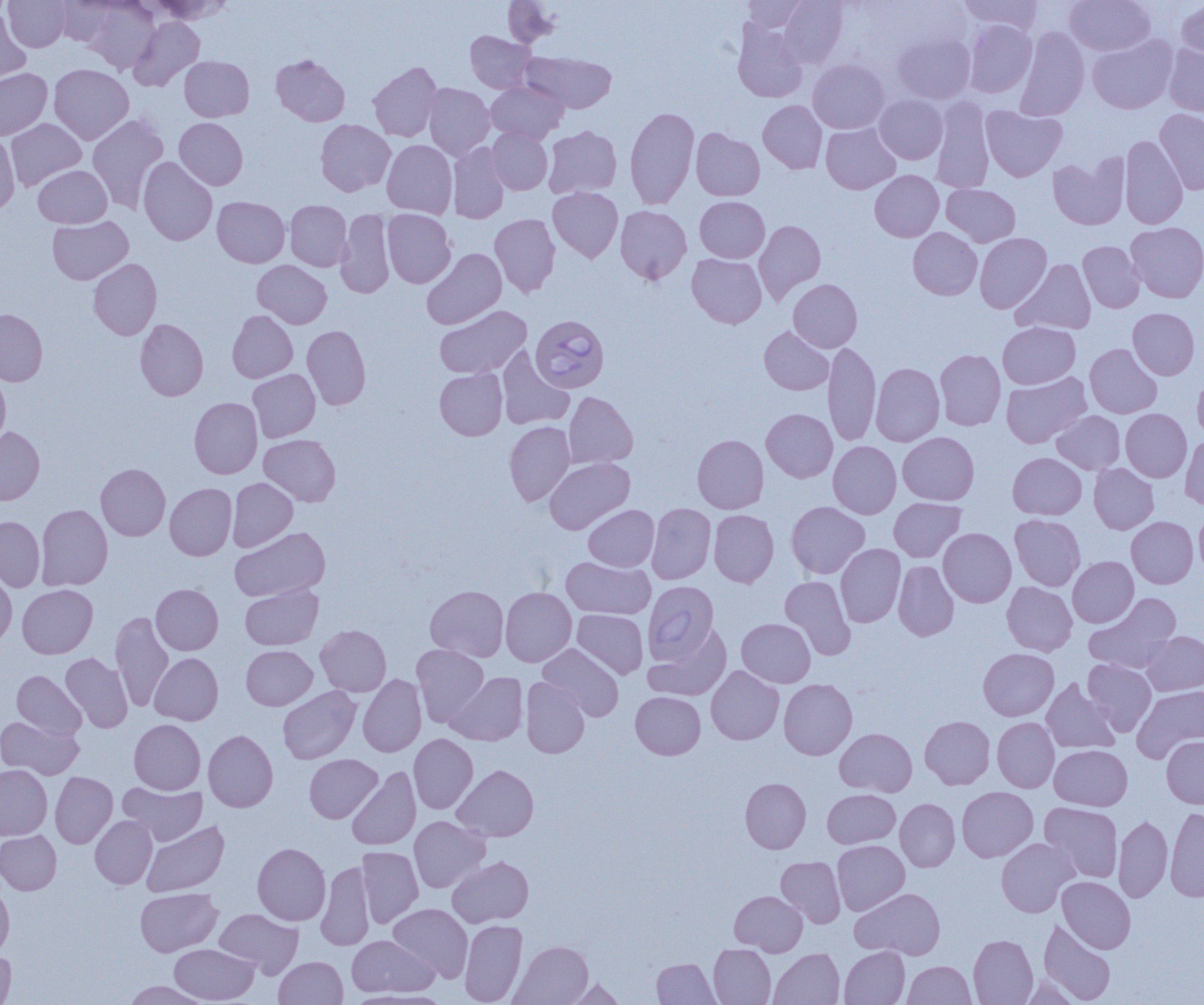
slide-level diagnosis = Babesia divergens
magnification = 1000x
field of view = single
image size = 1204×1005 pixels
Babesia divergens-infected red blood cell locations = approximate bounding boxes as (x1,y1)-(x2,y2) corner pairs in pixels: (531,314)-(610,392), (643,582)-(719,664)
preparation = thin blood smear
modality = optical microscopy
uninfected red blood cell locations = approximate bounding boxes as (x1,y1)-(x2,y2) corner pairs in pixels: (3,0)-(70,52), (54,0)-(117,46), (147,0)-(232,24), (503,0)-(560,48), (743,0)-(809,32), (779,0)-(847,67), (958,0)-(1042,36), (1065,0)-(1155,55), (83,1)-(160,73), (1177,1)-(1204,66), (0,9)-(31,86), (129,17)-(204,91), (963,20)-(1036,97), (732,21)-(808,102), (1014,27)-(1089,121), (465,31)-(535,93), (893,33)-(976,104), (1087,34)-(1177,113), (1163,44)-(1204,117), (522,51)-(617,113), (271,54)-(350,126), (180,56)-(254,121), (808,59)-(889,133), (368,62)-(442,141), (49,64)-(133,144), (0,68)-(52,140), (486,81)-(567,143), (423,83)-(495,159), (874,95)-(948,164), (930,97)-(994,193), (758,100)-(827,174), (981,105)-(1067,181), (624,106)-(699,209), (1155,109)-(1204,194), (87,114)-(169,212), (6,118)-(86,190), (174,118)-(247,189), (316,119)-(395,196), (821,123)-(900,194), (543,125)-(621,199), (487,128)-(552,194), (691,128)-(765,200), (0,132)-(20,216), (1120,135)-(1188,229), (382,139)-(457,218), (448,142)-(510,224), (1048,153)-(1129,230), (138,157)-(217,246), (33,165)-(111,228), (870,170)-(944,241), (941,184)-(1020,246), (548,187)-(623,262), (212,196)-(290,267), (695,196)-(769,262), (285,200)-(352,271), (615,205)-(692,284), (335,209)-(395,298), (383,209)-(456,288), (490,214)-(560,297), (48,216)-(133,284), (754,220)-(825,303), (1127,222)-(1204,302), (908,227)-(982,300), (975,233)-(1052,313), (1078,241)-(1145,312), (422,248)-(507,329), (687,253)-(766,328), (88,259)-(162,340), (1012,259)-(1096,334), (252,260)-(331,328), (788,279)-(863,352), (435,305)-(531,379), (1128,308)-(1200,380), (0,309)-(47,386), (228,310)-(297,382), (135,319)-(208,401), (998,322)-(1080,389), (302,325)-(371,409), (759,327)-(833,395), (823,341)-(881,446), (1085,344)-(1161,418), (496,347)-(574,430), (935,350)-(1005,430), (871,362)-(944,446), (435,368)-(507,440), (248,369)-(320,442), (1193,371)-(1204,443), (0,372)-(10,449), (1002,372)-(1091,448), (563,391)-(638,469), (189,397)-(262,478), (761,408)-(837,482), (1121,409)-(1192,482), (1052,410)-(1125,474), (504,421)-(575,505), (0,427)-(44,505), (898,432)-(979,505), (259,434)-(340,506), (1181,434)-(1204,510), (693,435)-(768,513), (828,441)-(901,519), (1008,452)-(1086,519), (545,457)-(634,534), (96,463)-(170,540), (1089,463)-(1158,534), (227,478)-(298,551), (165,483)-(237,560), (889,498)-(965,562), (786,501)-(869,579), (646,503)-(716,584), (36,504)-(113,590), (583,505)-(659,571), (1194,507)-(1204,579), (709,510)-(778,587), (1010,514)-(1085,590), (0,516)-(45,591), (1127,516)-(1198,588), (230,527)-(330,601), (938,528)-(1016,607), (835,543)-(905,627), (561,556)-(655,619), (1068,556)-(1139,627), (893,560)-(958,640), (0,572)-(17,649), (780,576)-(856,659), (1002,582)-(1077,656), (17,584)-(98,658), (151,584)-(223,655), (240,584)-(323,650), (425,585)-(509,662), (500,587)-(576,667), (1084,594)-(1181,673), (572,609)-(648,679), (110,611)-(174,711), (737,618)-(815,687), (316,625)-(391,696), (645,625)-(731,701), (1142,631)-(1204,696), (538,643)-(624,721), (411,644)-(489,726), (242,645)-(317,710), (978,648)-(1058,720), (61,653)-(133,732), (149,653)-(223,725), (1083,659)-(1156,736), (706,666)-(784,745), (12,671)-(86,739), (446,672)-(527,745), (358,674)-(426,756), (520,677)-(590,758), (779,678)-(857,759), (1042,678)-(1121,754), (1132,685)-(1204,762), (278,686)-(361,763), (631,692)-(705,759), (920,716)-(994,789), (0,717)-(83,780), (992,717)-(1060,792), (129,719)-(205,794), (835,728)-(916,796), (203,730)-(277,812), (409,734)-(477,813), (1162,736)-(1204,808), (1049,745)-(1132,810), (305,754)-(382,823), (453,764)-(538,842), (0,765)-(52,840), (347,767)-(420,850), (50,772)-(117,848), (740,778)-(811,853), (119,782)-(207,845), (957,787)-(1038,862), (823,789)-(900,848), (895,798)-(960,871), (1040,802)-(1123,882), (1165,807)-(1204,901), (90,815)-(157,889), (409,816)-(489,893), (1113,816)-(1172,902), (142,820)-(229,896), (0,830)-(61,895), (997,838)-(1078,917), (832,840)-(909,915), (252,843)-(330,925), (357,846)-(423,928), (448,856)-(534,928), (776,856)-(845,927), (316,861)-(375,951), (1057,876)-(1135,953), (0,881)-(14,960), (135,887)-(222,956), (851,888)-(946,959), (729,891)-(807,955), (389,903)-(472,981), (214,908)-(302,977), (460,919)-(527,1005), (1038,919)-(1116,1004), (968,934)-(1038,1005), (346,935)-(439,997), (509,940)-(593,1005), (170,943)-(258,1004), (709,944)-(775,1004), (839,946)-(909,1005), (768,948)-(844,1005), (0,949)-(16,1004), (275,956)-(348,1005), (652,958)-(720,1004), (903,960)-(976,1005), (1018,975)-(1082,1005), (564,978)-(626,1005), (124,981)-(211,1004), (347,989)-(451,1004)